Point out each Plasmodium parasite.
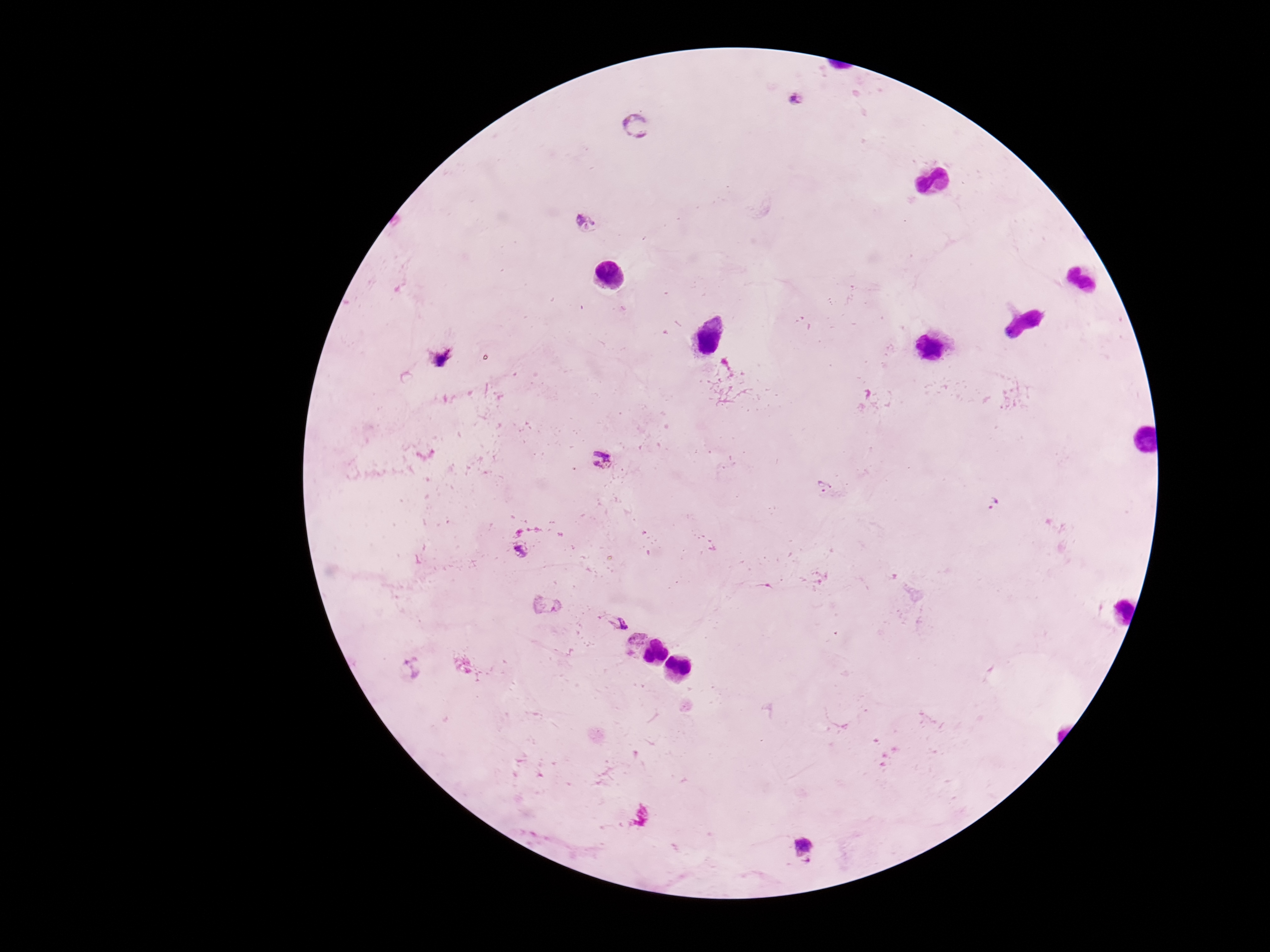
Approximate centers as {x, y} in pixels.
Plasmodium parasites: {798, 99}, {637, 124}, {585, 224}, {441, 358}, {602, 460}, {994, 505}, {519, 549}, {613, 621}, {803, 850}.

Summary:
  - Field of view: one from this slide
  - Image size: 1270×952 pixels
  - Preparation: thick blood film
  - Stain: Giemsa
  - Magnification: 100x
  - Capture: smartphone camera through the microscope eyepiece
  - Patient malaria status: positive